Outline every leukocyte.
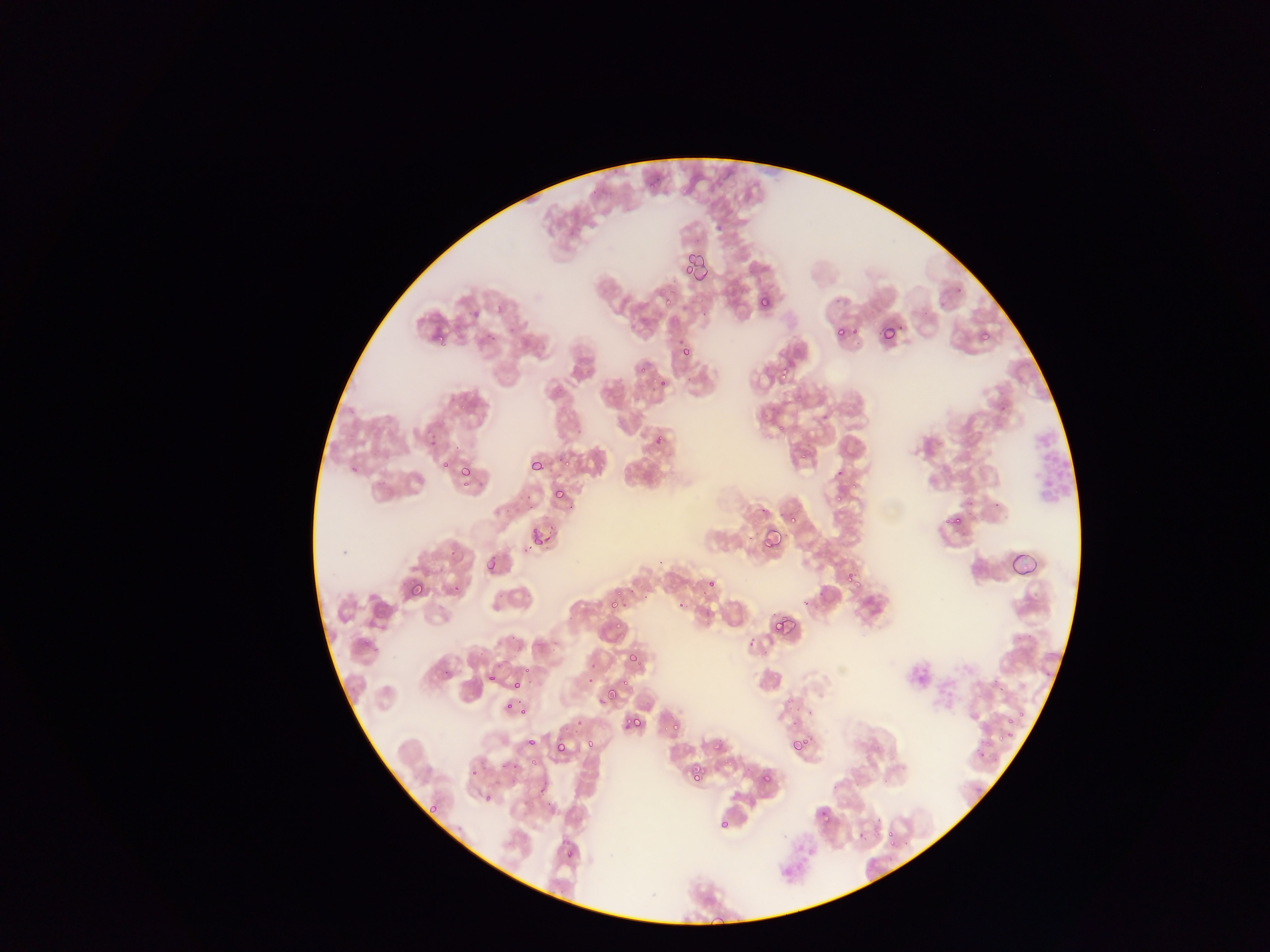

Approximate bounding boxes as [left, top, right, bottom] in pixels.
Leukocytes: [1032, 420, 1076, 509].

Malaria parasite locations: [644, 168, 658, 191], [680, 253, 696, 268], [694, 256, 711, 286], [680, 264, 695, 277], [683, 267, 692, 277], [659, 295, 676, 310], [759, 295, 771, 309], [879, 323, 897, 343], [833, 325, 845, 337], [849, 325, 859, 336], [432, 331, 444, 342], [979, 331, 990, 340], [679, 346, 691, 358], [636, 363, 647, 374], [778, 363, 792, 377], [658, 377, 667, 387], [652, 431, 665, 449], [796, 447, 810, 463], [560, 454, 576, 469], [442, 459, 453, 470], [531, 460, 543, 470], [349, 466, 358, 473], [461, 467, 471, 478], [849, 480, 860, 492], [459, 481, 470, 490], [553, 488, 565, 500], [827, 490, 844, 509], [947, 512, 964, 528], [786, 513, 798, 524], [760, 526, 781, 549], [530, 533, 547, 553], [485, 561, 497, 574], [846, 572, 862, 590], [707, 579, 716, 588], [408, 580, 426, 599], [450, 582, 461, 594], [609, 600, 618, 610], [677, 602, 686, 611], [771, 616, 787, 633], [613, 617, 627, 635], [748, 634, 759, 649], [628, 652, 639, 663], [521, 663, 532, 677], [487, 672, 496, 682], [616, 676, 636, 695], [514, 680, 524, 690], [607, 690, 619, 703], [505, 700, 515, 711], [519, 707, 528, 717], [1002, 714, 1025, 727], [628, 715, 642, 729], [671, 721, 681, 732], [997, 723, 1014, 748], [662, 727, 670, 738], [789, 735, 807, 753], [526, 737, 536, 746], [585, 739, 595, 748], [553, 740, 567, 755], [712, 740, 725, 752], [976, 743, 990, 765], [501, 762, 509, 771], [689, 766, 703, 782], [469, 768, 477, 779], [762, 772, 772, 782], [483, 793, 493, 803], [429, 803, 439, 812], [819, 809, 830, 820], [718, 818, 729, 828], [886, 831, 897, 843], [565, 849, 575, 860]. Collected in Ghana. Image is 1270×952 pixels. Mobile-phone photograph taken through the microscope. One field of view. Thin blood smear.